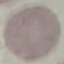

malaria status = uninfected
capture = smartphone through the microscope eyepiece
preparation = thin blood film
stain = Giemsa
image type = automatically extracted cell patch, resized to 64 × 64 pixels